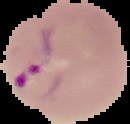
{
  "image_size": "130×124 pixels",
  "result": "Plasmodium parasites identified",
  "preparation": "thin blood smear",
  "image_type": "segmented cell region on a black background"
}